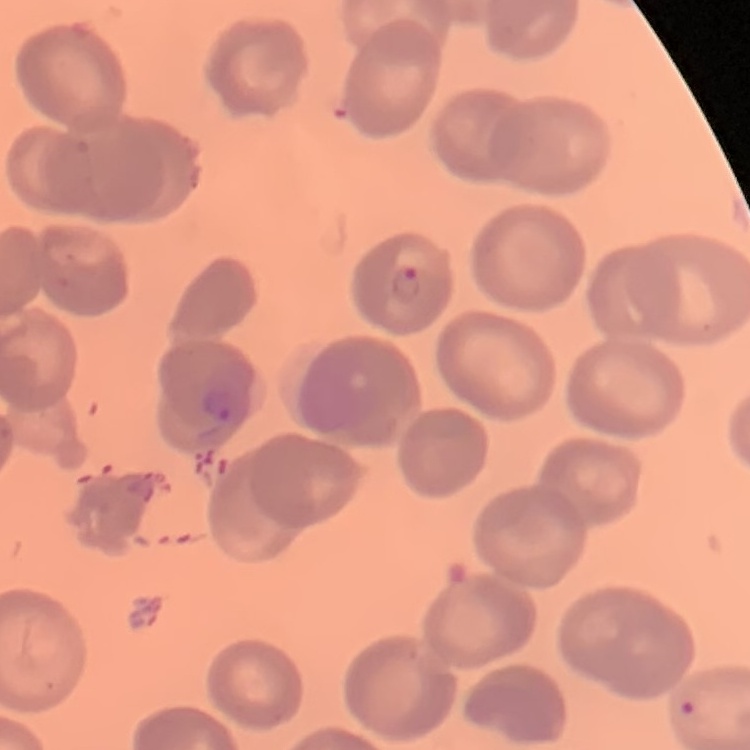 The erythrocytes show no rouleaux formation. Stained with either Field's or Giemsa. Square crop of a larger photomicrograph. Thin peripheral smear.